State the preparation type.
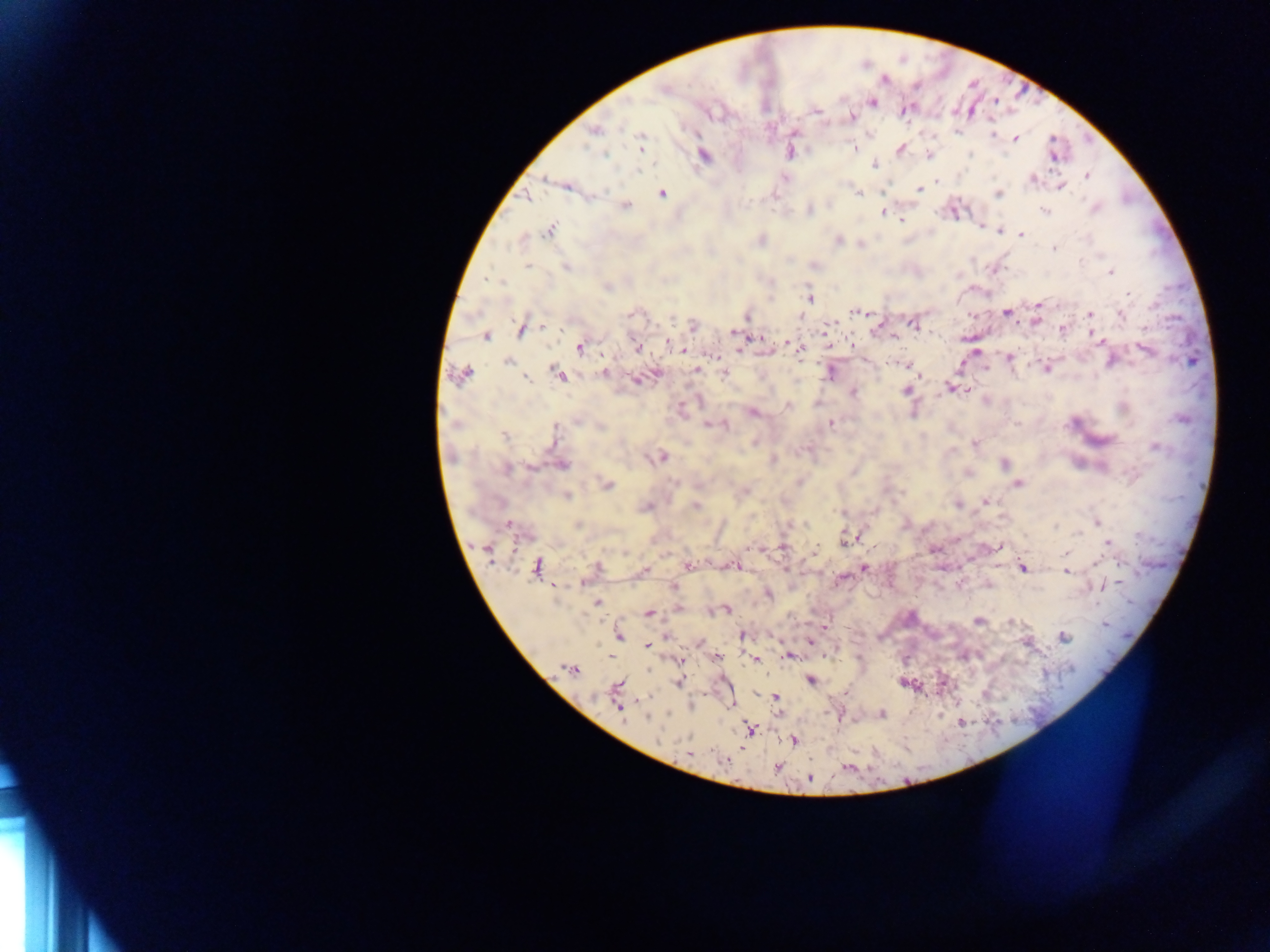

Thick blood film.

Approximate centers as (x, y) in pixels.
Summary:
  - Plasmodium parasite locations: (664, 90), (872, 102), (815, 111), (851, 117), (594, 131), (992, 134), (640, 137), (1014, 138), (640, 147), (900, 148), (855, 149), (790, 153), (605, 155), (705, 156), (874, 165), (639, 171), (1087, 175), (546, 179), (1033, 180), (937, 182), (1061, 186), (568, 187), (919, 189), (662, 193), (859, 193), (998, 193), (525, 197), (625, 206), (1095, 208), (809, 211), (1045, 211), (883, 212), (901, 220), (981, 227), (550, 231), (998, 232), (1021, 235), (762, 240), (838, 240), (1054, 248), (528, 266), (566, 267), (994, 270), (1111, 272), (487, 279), (607, 287), (1128, 294), (810, 299), (1039, 305), (854, 311), (1006, 313), (631, 315), (869, 315), (1090, 315), (1121, 315), (747, 317), (799, 317), (1036, 321), (914, 324), (693, 325), (543, 327), (1062, 329), (521, 330), (735, 333), (753, 336), (486, 337), (893, 337), (1095, 337), (758, 338), (668, 343), (790, 345), (852, 345), (579, 348), (636, 348), (740, 349), (799, 349), (1145, 350), (685, 351), (1009, 358), (1110, 361), (507, 362), (899, 364), (906, 365), (1046, 367), (696, 370), (830, 372), (604, 373), (558, 374), (463, 375), (724, 375), (920, 375), (528, 379), (637, 380), (952, 389), (906, 390), (965, 390), (853, 392), (788, 406), (753, 413), (577, 420), (1181, 420), (456, 424), (831, 424), (707, 425), (725, 425), (600, 427), (504, 436), (974, 444), (1156, 447), (663, 457), (773, 460), (1004, 463), (562, 465), (531, 468), (507, 469), (607, 484), (1018, 484), (568, 496), (985, 502), (957, 505), (695, 506), (647, 507), (1097, 523), (805, 524), (578, 525), (509, 526), (1055, 526), (1080, 533), (848, 539), (1108, 542), (782, 547), (999, 547), (815, 549), (487, 550), (1065, 553), (1098, 563), (688, 565), (735, 566), (537, 567), (597, 568), (864, 568), (1023, 568), (645, 570), (1067, 571), (674, 587), (598, 602), (678, 608), (726, 610), (649, 613), (979, 621), (1011, 622), (1105, 625), (824, 627), (619, 635), (742, 635), (666, 636), (1063, 638), (810, 643), (646, 646), (790, 656), (718, 658), (680, 660), (755, 661), (571, 668), (810, 681), (678, 683), (617, 686), (776, 697), (619, 707), (882, 714), (646, 717), (749, 729), (793, 740), (689, 753), (725, 761), (777, 767), (810, 778)
  - Image size: 1270×952 pixels
  - Country: Ghana
  - Capture: mobile-phone photograph through a microscope
  - Field of view: single